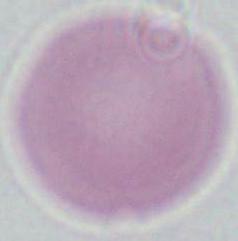

1000x magnification. A red blood cell is shown. Micrograph.